Name the parasite shown.
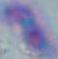

This is Toxoplasma gondii.

Summary:
  - Modality: micrograph
  - Magnification: 1000x